State which parasite is depicted.
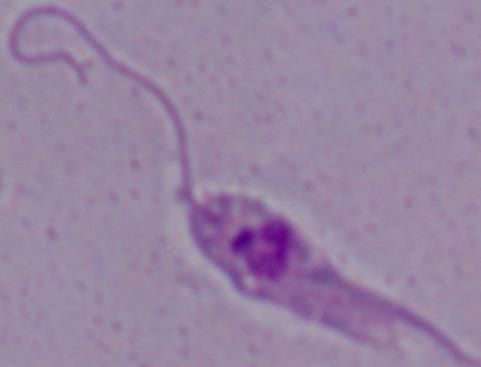
Leishmania.

Captured at 1000x magnification. Photomicrograph.